Assess the morphology of the red blood cells.
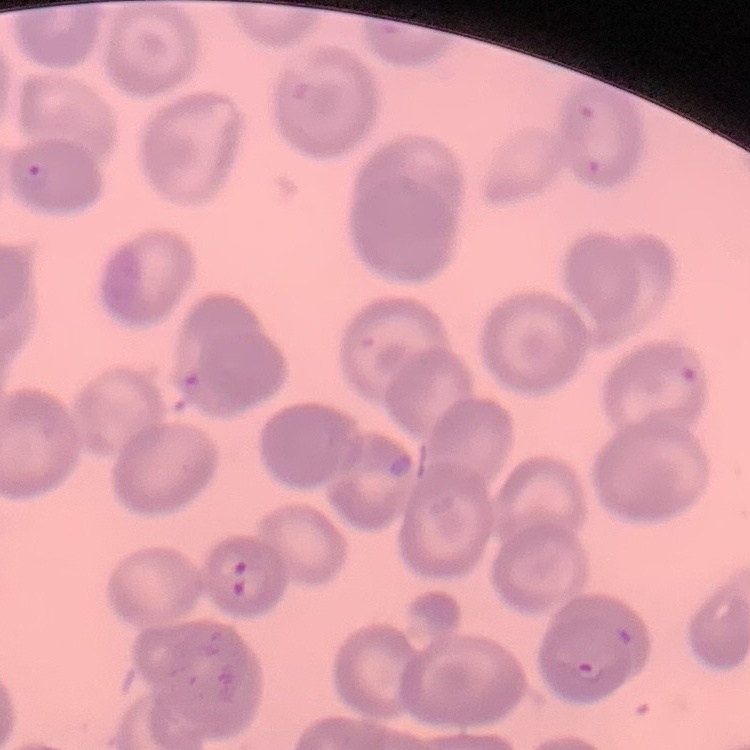

No rouleaux formation.

Summary:
  - Preparation: thin peripheral smear
  - Image type: square crop of a larger photomicrograph
  - Stain: Field's or Giemsa